Locate every blood parasite and identify its species.
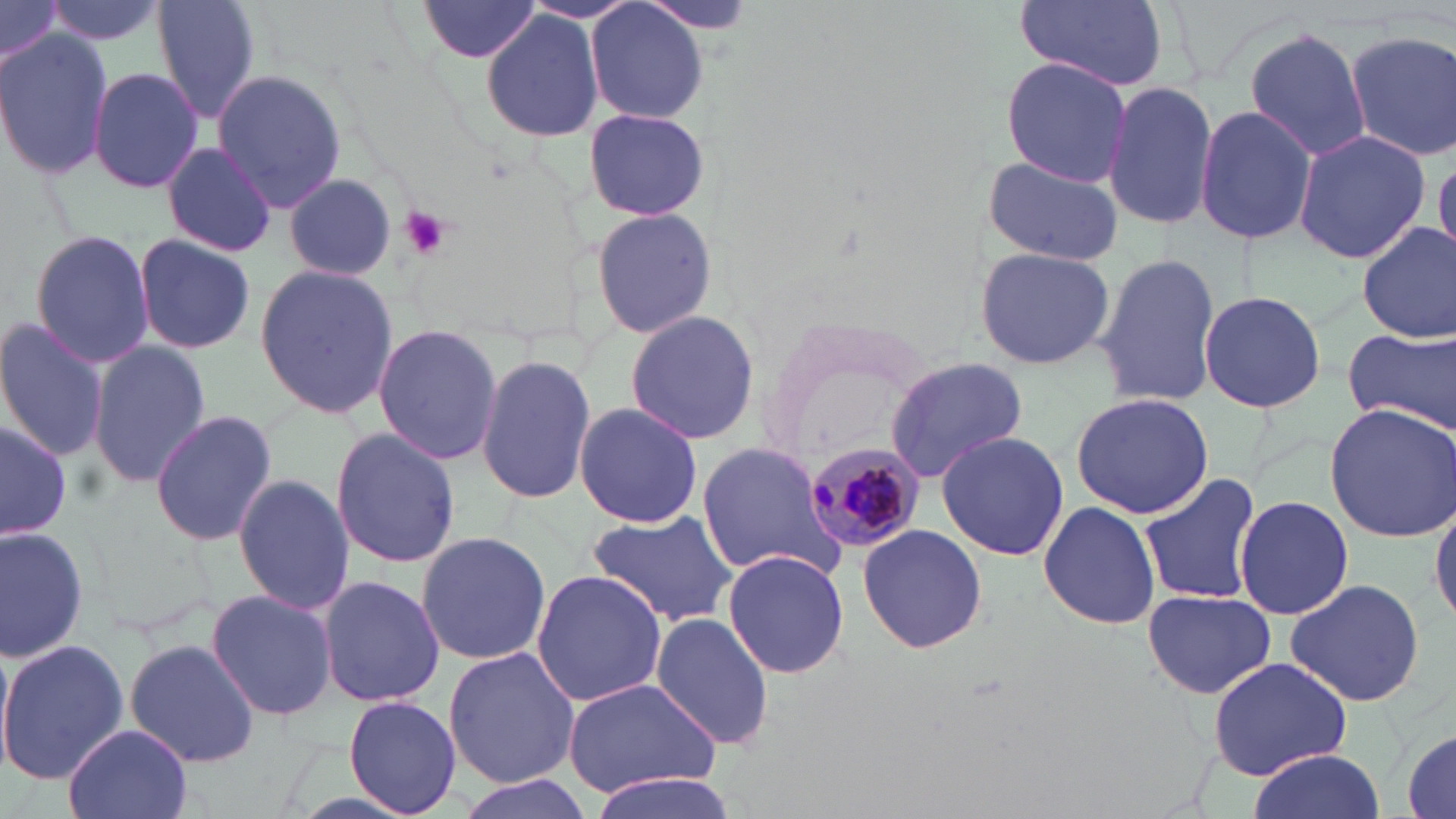

Approximate bounding boxes as [x1, y1, x2, y2] in pixels.
Plasmodium malariae-infected red blood cells: [806, 435, 921, 551].
No Plasmodium falciparum, Plasmodium ovale, Plasmodium vivax, Babesia divergens, or Trypanosoma brucei observed.

slide-level diagnosis = Plasmodium malariae
uninfected red blood cell locations = approximate bounding boxes as [x1, y1, x2, y2] in pixels: [0, 0, 62, 72], [44, 0, 163, 46], [153, 0, 261, 124], [416, 0, 550, 68], [1015, 0, 1173, 92], [586, 2, 708, 126], [481, 11, 604, 141], [1244, 26, 1372, 162], [1345, 28, 1456, 163], [0, 29, 111, 179], [999, 57, 1133, 185], [88, 65, 204, 194], [212, 69, 348, 212], [1102, 79, 1219, 230], [1195, 103, 1317, 247], [583, 105, 711, 223], [1292, 129, 1430, 264], [158, 141, 280, 259], [984, 154, 1126, 267], [1432, 154, 1455, 258], [284, 175, 397, 279], [588, 205, 720, 339], [1357, 220, 1456, 343], [30, 229, 155, 370], [133, 232, 256, 354], [974, 245, 1116, 371], [1096, 254, 1223, 405], [254, 262, 401, 421], [1198, 289, 1327, 414], [625, 309, 760, 445], [754, 313, 936, 467], [0, 318, 109, 463], [372, 323, 503, 467], [1342, 326, 1455, 433], [89, 341, 212, 486], [476, 355, 595, 506], [884, 357, 1030, 483], [1069, 392, 1213, 519], [573, 400, 703, 529], [1324, 404, 1456, 542], [148, 410, 277, 544], [0, 416, 74, 539], [333, 425, 459, 569], [934, 429, 1068, 562], [697, 442, 848, 582], [1139, 469, 1263, 609], [233, 473, 353, 617], [1235, 495, 1353, 618], [1038, 500, 1162, 631], [1430, 500, 1456, 626], [586, 509, 736, 630], [0, 523, 87, 662], [857, 523, 988, 653], [415, 531, 552, 665], [722, 548, 850, 680], [530, 569, 666, 708], [318, 574, 444, 709], [1283, 576, 1427, 708], [206, 588, 339, 723], [1141, 589, 1276, 701], [652, 610, 776, 752], [0, 637, 129, 786], [123, 637, 260, 767], [0, 640, 16, 775], [444, 646, 581, 787], [1206, 656, 1354, 786], [562, 678, 724, 799], [343, 695, 463, 818], [64, 723, 193, 819], [1401, 729, 1455, 818], [1246, 752, 1386, 819], [586, 770, 742, 819], [454, 773, 597, 819]
preparation = thin blood film
stain = May-Grünwald-Giemsa
field of view = single
magnification = 1000x
image size = 1456×819 pixels
platelet locations = approximate bounding boxes as [x1, y1, x2, y2] in pixels: [398, 206, 452, 260]
modality = optical microscopy